Report the malaria status of this cell.
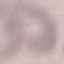
Uninfected.

image_type: automatically extracted cell patch, resized to 64 × 64 pixels
capture: smartphone camera at the microscope eyepiece
preparation: thin smear
stain: Giemsa